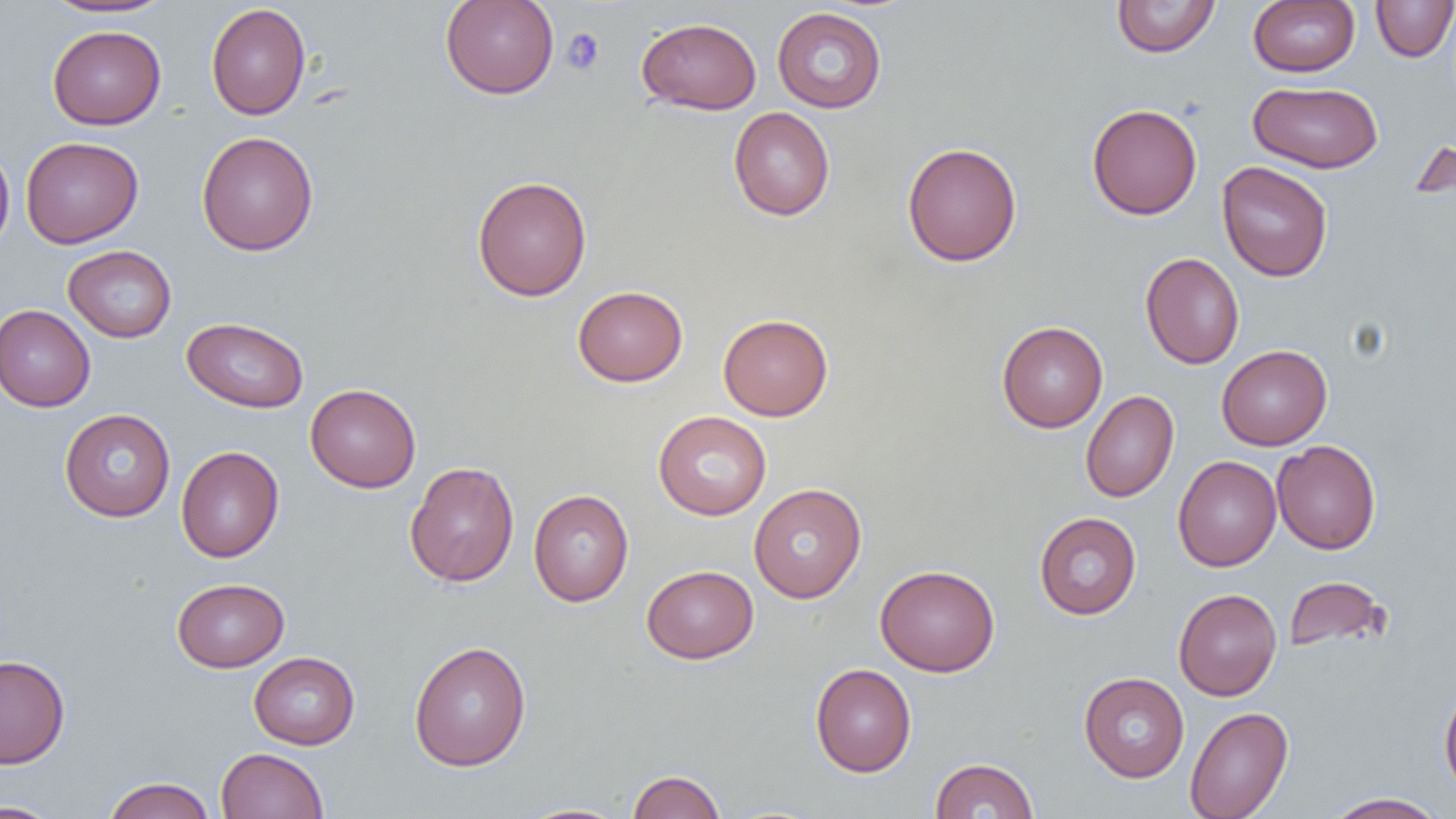
Summary:
  - Coordinate format: approximate bounding boxes as [x1, y1, x2, y2] in pixels
  - Platelet locations: [561, 28, 604, 75]
  - Uninfected red blood cell locations: [43, 0, 174, 18], [440, 0, 559, 99], [1112, 0, 1220, 57], [1248, 1, 1360, 77], [1371, 1, 1456, 62], [206, 3, 311, 120], [772, 6, 887, 113], [637, 17, 762, 114], [47, 25, 166, 130], [1247, 81, 1383, 173], [1086, 103, 1202, 220], [728, 106, 836, 221], [197, 131, 318, 256], [1410, 132, 1455, 206], [20, 136, 143, 248], [902, 142, 1022, 267], [0, 146, 15, 256], [1217, 161, 1333, 282], [472, 175, 592, 302], [63, 245, 176, 343], [1140, 252, 1245, 369], [572, 285, 688, 387], [0, 304, 95, 412], [718, 313, 833, 421], [182, 317, 308, 413], [997, 321, 1108, 433], [1216, 345, 1332, 450], [305, 383, 421, 493], [1080, 390, 1179, 502], [59, 408, 176, 521], [653, 411, 772, 520], [1272, 439, 1381, 554], [176, 446, 284, 562], [1173, 455, 1281, 571], [404, 461, 520, 587], [749, 483, 867, 603], [528, 489, 634, 606], [1034, 512, 1141, 619], [875, 564, 1000, 677], [641, 565, 758, 664], [1284, 575, 1389, 655], [172, 578, 289, 672], [1173, 588, 1282, 701], [409, 640, 531, 772], [249, 651, 360, 749], [0, 655, 70, 768], [810, 663, 916, 777], [1078, 672, 1189, 782], [1439, 682, 1456, 800], [1185, 705, 1293, 819], [216, 747, 329, 819], [930, 758, 1039, 818], [627, 770, 726, 818], [103, 777, 216, 819], [1324, 792, 1447, 819], [0, 800, 65, 819], [512, 803, 634, 819]
  - Slide-level diagnosis: no evidence of blood parasites
  - Modality: light microscopy
  - Field of view: single
  - Preparation: thin blood smear
  - Image size: 1456×819 pixels
  - Magnification: 1000x